Report the malaria status of this cell.
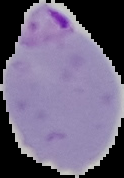
It is parasitized.

Summary:
  - Image type: cell region segmented out of the field of view; surrounding area masked to black
  - Preparation: thin blood smear
  - Image size: 124×178 pixels